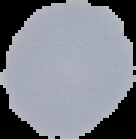
malaria status = uninfected
image size = 136×139 pixels
image type = cell region segmented out of the field of view; surrounding area masked to black
preparation = thin blood film